Locate every blood parasite and identify its species.
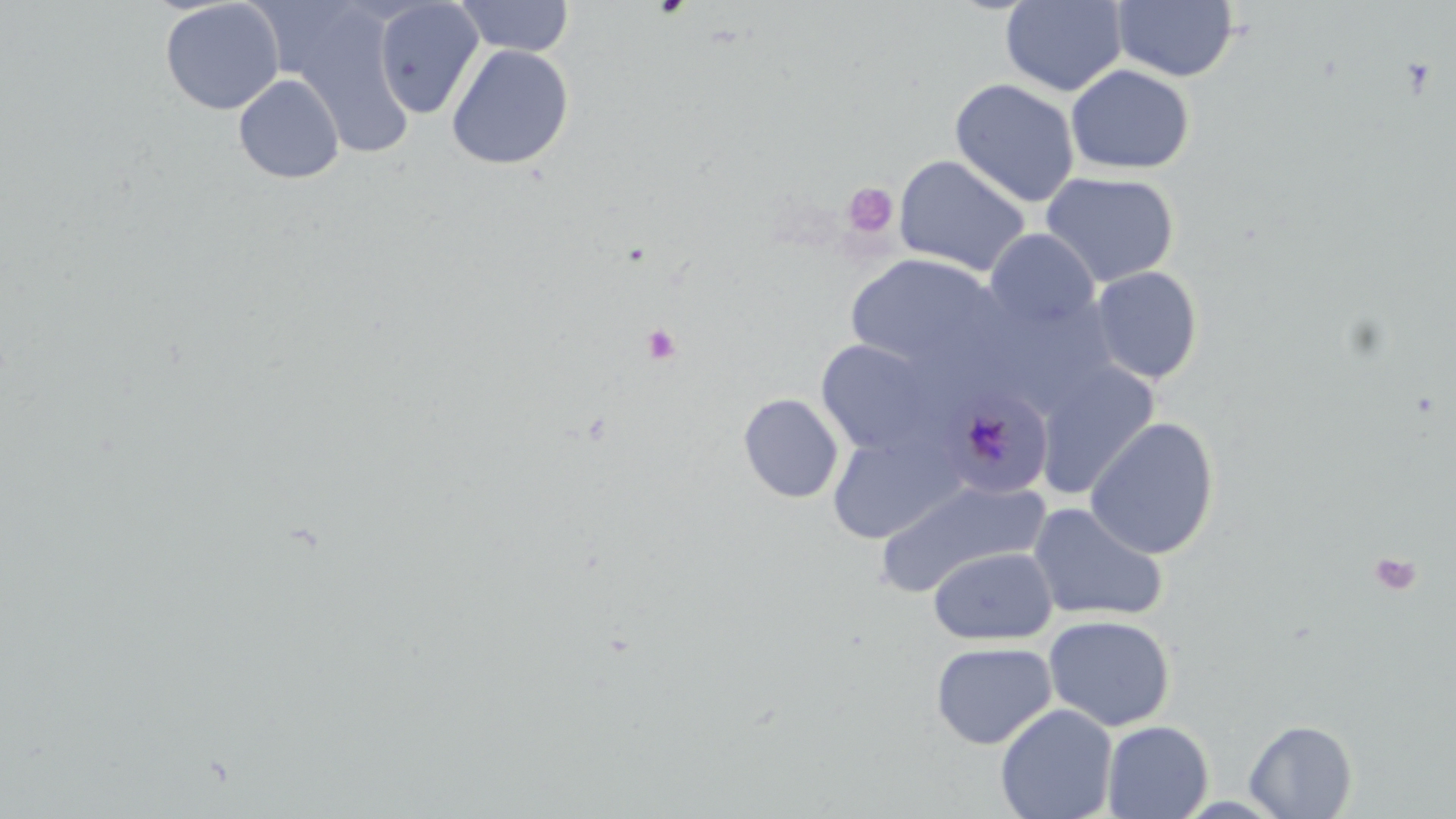
Approximate bounding boxes as [x1, y1, x2, y2] in pixels.
Plasmodium malariae-infected red blood cells: [941, 388, 1054, 498].
No Plasmodium falciparum, Plasmodium ovale, Plasmodium vivax, Babesia divergens, or Trypanosoma brucei observed.

Platelet locations: [843, 181, 899, 239], [640, 323, 682, 366], [1369, 549, 1422, 597]. Uninfected red blood cell locations: [160, 0, 285, 115], [453, 0, 575, 58], [1000, 0, 1128, 96], [1112, 0, 1239, 82], [374, 2, 484, 118], [287, 5, 416, 159], [446, 44, 574, 170], [1066, 64, 1195, 175], [232, 73, 345, 185], [950, 78, 1080, 207], [893, 154, 1032, 276], [1041, 171, 1180, 288], [985, 228, 1099, 332], [844, 253, 1008, 379], [1090, 266, 1203, 385], [815, 339, 944, 457], [1034, 362, 1159, 500], [738, 393, 843, 503], [1084, 416, 1220, 559], [827, 432, 966, 544], [875, 479, 1047, 596], [1027, 502, 1168, 622], [928, 546, 1058, 645], [1043, 614, 1176, 732], [930, 641, 1056, 750], [995, 703, 1118, 819], [1244, 719, 1357, 818], [1102, 720, 1213, 818]. Slide-level diagnosis: Plasmodium malariae. May-Grünwald-Giemsa-stained preparation. Optical microscopy. Captured at 1000x magnification. Single field of view. Thin blood film. Image is 1456×819 pixels.